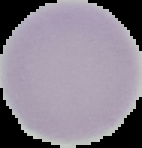

Image is 142×148 pixels. From a thin blood smear. Malaria status: uninfected. The area outside the segmented cell region is set to black.